Assess the morphology of the erythrocytes.
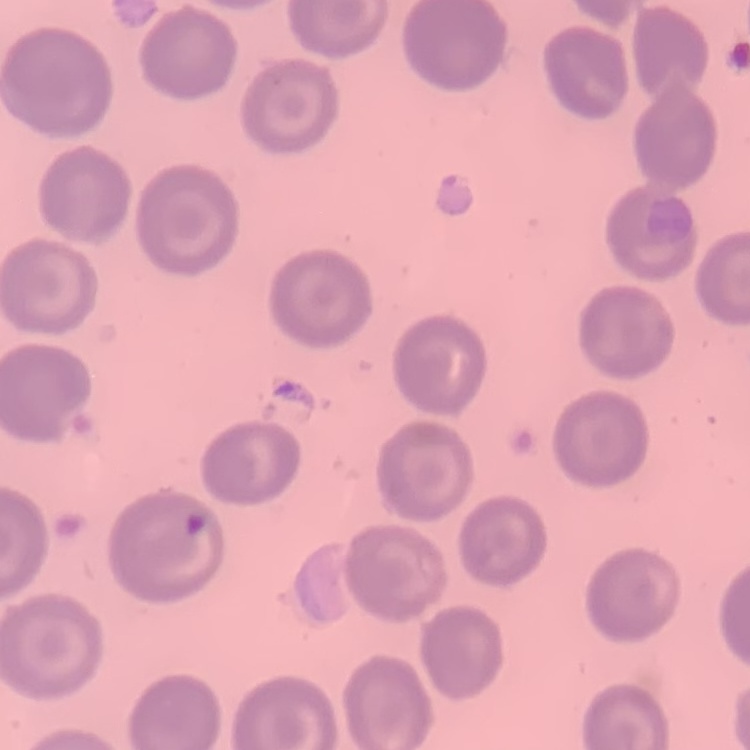

They show no rouleaux formation.

Summary:
  - Preparation: thin blood smear
  - Stain: Field's or Giemsa
  - Image type: one tile cut from a larger photomicrograph